Locate every leukocyte (white blood cell).
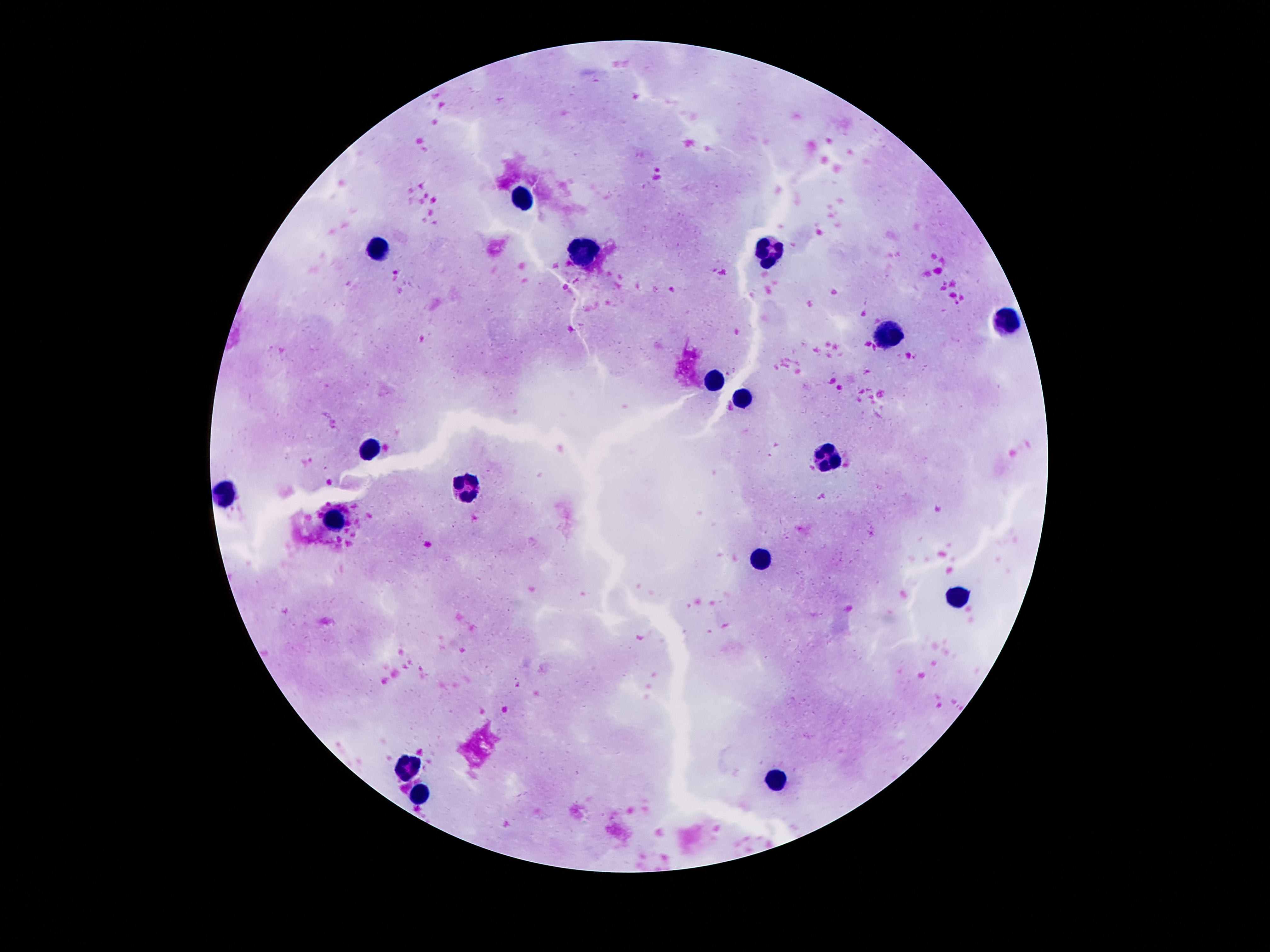
Approximate object centers, in pixels from the top-left corner.
Leukocytes: (x=523, y=196), (x=586, y=251), (x=374, y=253), (x=769, y=255), (x=1006, y=323), (x=886, y=335), (x=714, y=379), (x=742, y=398), (x=370, y=449), (x=826, y=457), (x=466, y=490), (x=227, y=495), (x=336, y=520), (x=760, y=558), (x=956, y=595), (x=410, y=765), (x=775, y=782), (x=422, y=793).

Smartphone photograph taken through the microscope eyepiece. 100x magnification. Patient malaria status: uninfected. Image is 1270×952 pixels. Giemsa-stained preparation. One field from this slide. Thick blood smear.